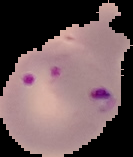

Result: malaria parasites detected. Segmented cell region on a black background. From a thin blood film. Image is 133×157 pixels.